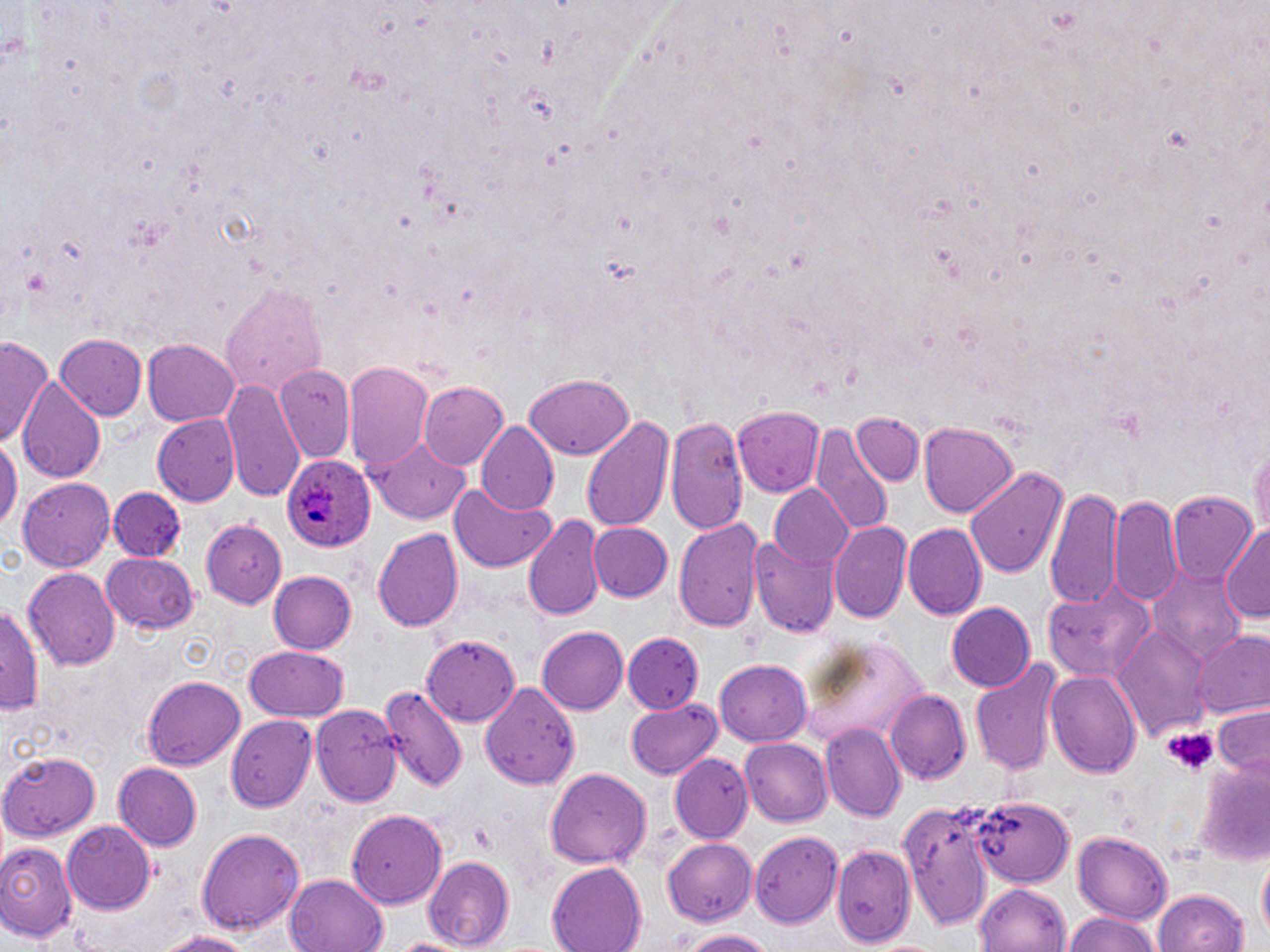
Approximate bounding boxes as (x1, y1, x2, y2) in pixels. Plasmodium ovale-infected red blood cell locations: (280, 454, 375, 555). Platelet locations: (1161, 727, 1217, 776). Uninfected red blood cell locations: (220, 279, 328, 398), (54, 334, 147, 422), (0, 339, 56, 446), (143, 340, 240, 427), (345, 361, 436, 476), (274, 366, 354, 460), (523, 372, 636, 459), (221, 376, 306, 506), (18, 377, 104, 480), (419, 380, 511, 470), (547, 381, 675, 497), (738, 405, 825, 494), (153, 414, 239, 505), (852, 414, 923, 488), (582, 415, 674, 534), (666, 416, 748, 533), (919, 420, 1019, 517), (812, 421, 894, 538), (476, 423, 558, 517), (0, 434, 18, 539), (372, 439, 470, 524), (1248, 439, 1270, 543), (964, 466, 1070, 579), (20, 475, 117, 568), (448, 483, 559, 574), (770, 486, 857, 570), (1045, 488, 1121, 608), (109, 489, 187, 560), (1110, 491, 1182, 607), (1168, 492, 1258, 584), (522, 515, 605, 623), (674, 516, 766, 634), (200, 519, 287, 609), (828, 520, 911, 622), (588, 522, 673, 603), (900, 522, 987, 619), (1220, 525, 1270, 626), (373, 526, 465, 635), (750, 532, 839, 636), (103, 551, 199, 635), (22, 565, 119, 666), (1151, 570, 1248, 659), (267, 571, 358, 655), (1043, 578, 1156, 679), (1, 601, 46, 715), (946, 602, 1036, 693), (537, 627, 627, 715), (1116, 627, 1212, 737), (1193, 631, 1270, 722), (621, 632, 704, 714), (423, 633, 520, 725), (799, 638, 935, 744), (244, 644, 349, 724), (717, 657, 816, 744), (970, 659, 1064, 779), (1046, 668, 1141, 781), (141, 676, 245, 771), (483, 681, 581, 789), (379, 682, 467, 796), (885, 689, 971, 787), (626, 699, 723, 779), (314, 706, 403, 807), (1210, 706, 1270, 776), (226, 714, 321, 810), (822, 724, 907, 823), (740, 737, 833, 825), (0, 751, 102, 840), (668, 754, 753, 843), (1193, 761, 1269, 864), (113, 763, 203, 849), (545, 767, 652, 869), (971, 795, 1076, 887), (897, 802, 1001, 929), (347, 809, 451, 908), (60, 822, 156, 913), (194, 826, 306, 936), (749, 829, 843, 928), (1073, 830, 1173, 923), (663, 837, 757, 927), (830, 840, 921, 949), (0, 842, 77, 946), (423, 856, 514, 951), (1255, 857, 1268, 946), (547, 862, 648, 952), (284, 874, 390, 952), (974, 884, 1072, 952), (1149, 889, 1251, 952), (1061, 911, 1163, 952), (152, 927, 256, 952), (678, 928, 774, 951), (385, 935, 479, 952). Slide-level diagnosis: Plasmodium ovale. Captured at 1000x magnification. May-Grünwald-Giemsa-stained preparation. Thin blood smear. Image is 1270×952 pixels. One field of a larger specimen. Optical microscopy.